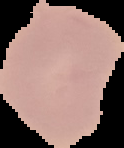

From a thin blood smear. Malaria status: uninfected. Image is 124×148 pixels. Cell region segmented out of the field of view; the surrounding area is masked to black.